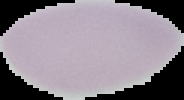

image type = cell region segmented out of the field of view; surrounding area masked to black
malaria status = uninfected
image size = 184×100 pixels
preparation = thin blood smear